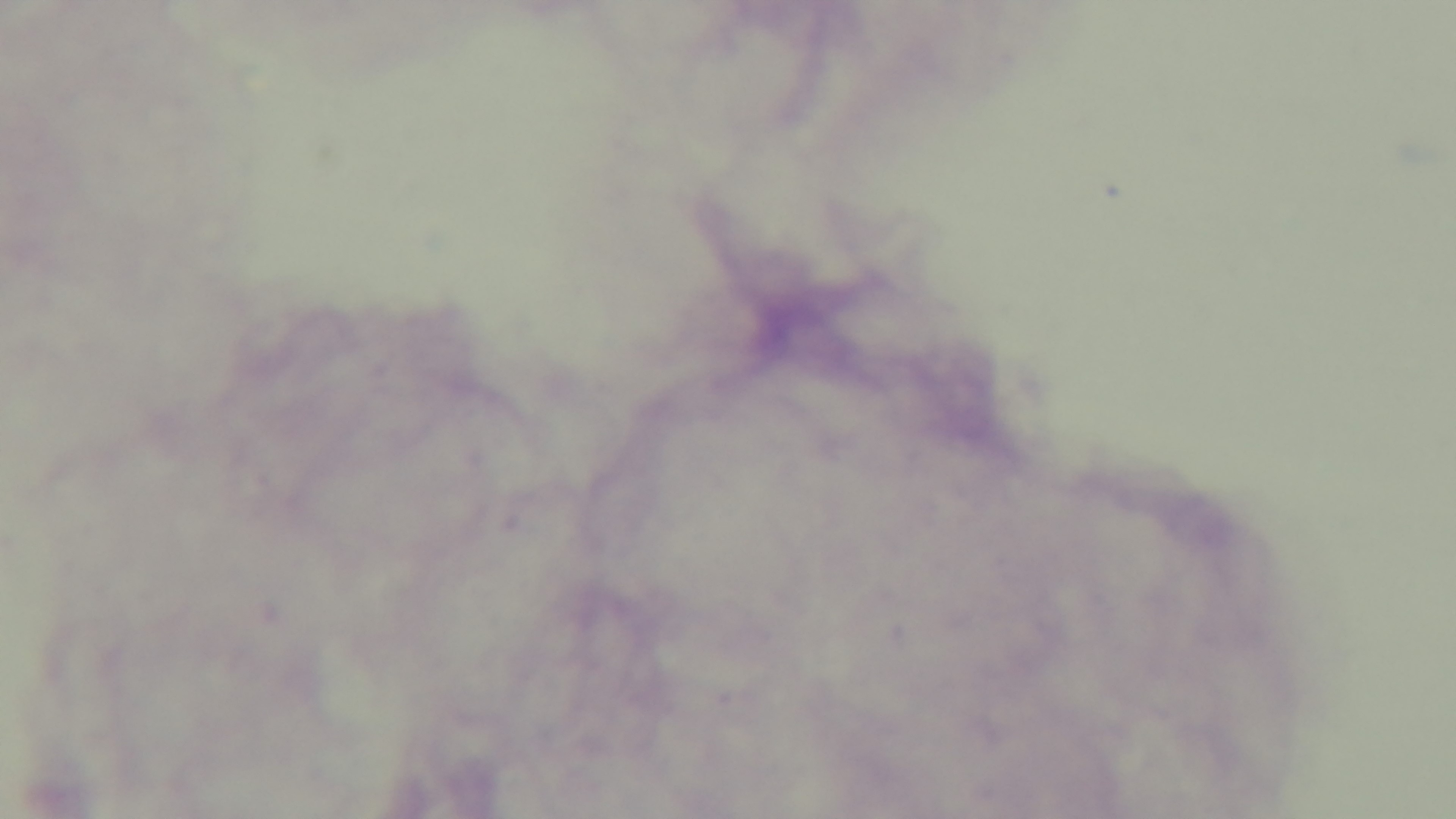
Summary:
  - Stain: Giemsa
  - Preparation: thick blood film
  - Objective: 100x oil immersion
  - Field of view: single
  - Modality: light microscopy
  - Malaria status: uninfected
  - Capture: mounted 4K digital camera